Locate every Plasmodium falciparum-infected red blood cell.
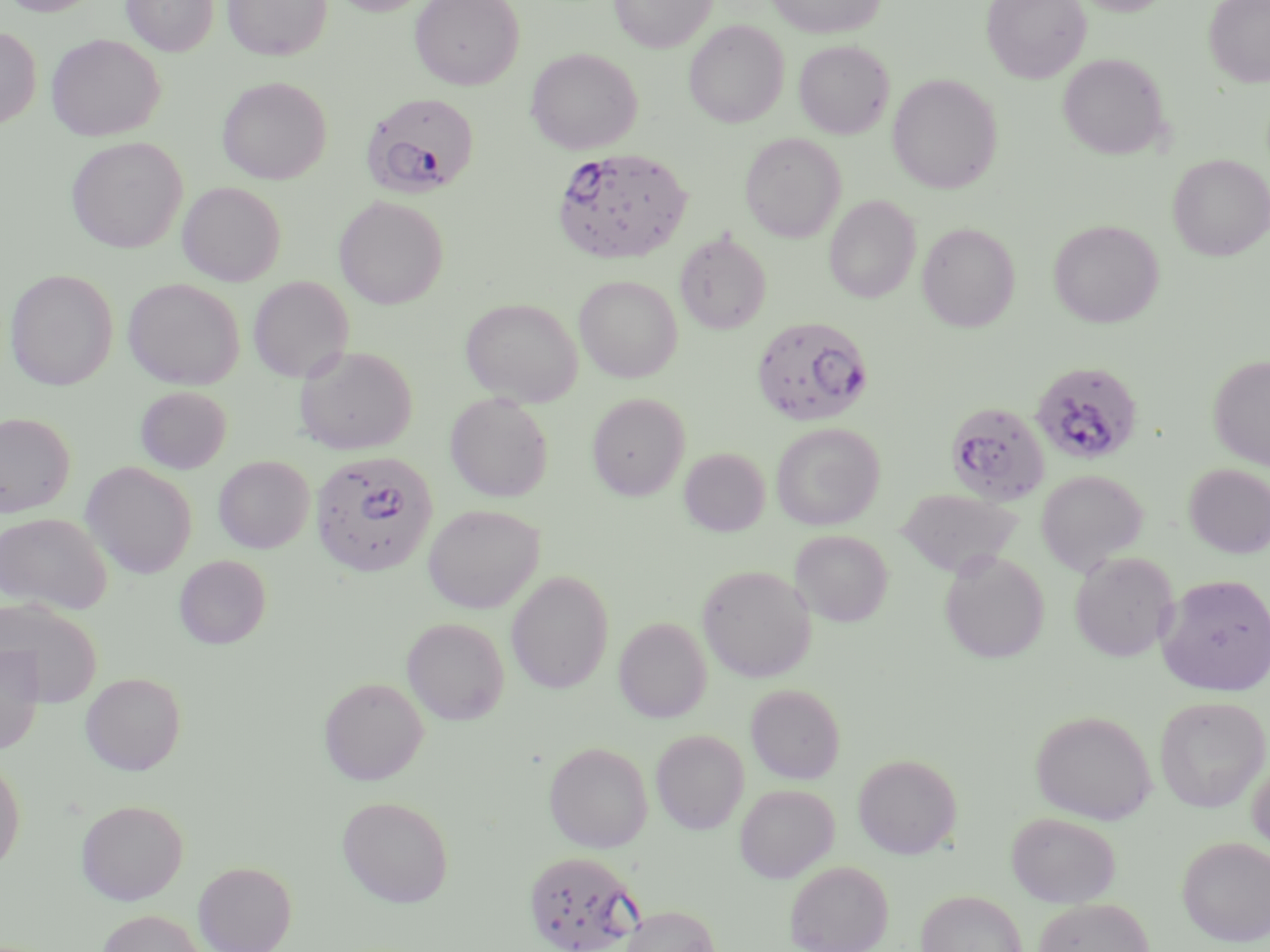

Approximate bounding boxes as (x1, y1, x2, y2) in pixels.
Plasmodium falciparum-infected red blood cells: (361, 92, 478, 198), (550, 147, 693, 264), (751, 315, 873, 427), (1029, 360, 1144, 467), (944, 400, 1052, 503), (310, 450, 438, 578), (523, 849, 642, 952).

Uninfected red blood cell locations: (3, 0, 101, 16), (122, 0, 219, 56), (223, 0, 331, 61), (329, 0, 435, 15), (410, 0, 524, 89), (610, 0, 715, 53), (767, 0, 885, 38), (982, 0, 1091, 83), (1071, 0, 1176, 15), (1204, 0, 1270, 87), (684, 20, 789, 128), (0, 27, 42, 129), (46, 34, 164, 141), (794, 40, 893, 138), (526, 47, 643, 154), (1057, 53, 1170, 159), (887, 73, 1003, 194), (217, 77, 331, 184), (739, 132, 846, 242), (66, 137, 187, 254), (1168, 154, 1270, 260), (177, 181, 286, 286), (824, 195, 920, 303), (334, 196, 449, 309), (1048, 219, 1164, 328), (917, 222, 1020, 332), (675, 231, 771, 334), (4, 269, 118, 390), (574, 275, 683, 383), (247, 276, 354, 383), (124, 278, 244, 389), (460, 298, 582, 406), (294, 345, 418, 454), (1207, 354, 1270, 470), (135, 386, 232, 474), (445, 392, 554, 502), (587, 392, 690, 500), (0, 412, 76, 518), (771, 422, 885, 530), (679, 448, 770, 536), (213, 456, 315, 553), (81, 461, 197, 579), (1183, 463, 1270, 558), (1036, 470, 1147, 574), (896, 488, 1023, 577), (423, 504, 544, 613), (0, 513, 112, 614), (790, 529, 893, 627), (939, 549, 1050, 663), (1070, 551, 1178, 661), (174, 555, 271, 649), (698, 565, 815, 682), (506, 570, 614, 694), (1157, 573, 1270, 696), (0, 601, 102, 706), (402, 617, 510, 725), (614, 617, 712, 722), (0, 645, 44, 753), (81, 672, 186, 775), (319, 677, 429, 785), (746, 683, 846, 783), (1155, 696, 1270, 812), (1030, 710, 1156, 824), (651, 728, 750, 834), (544, 741, 653, 853), (853, 753, 962, 859), (0, 756, 25, 873), (1247, 758, 1270, 861), (734, 784, 838, 883), (337, 795, 454, 908), (76, 799, 189, 905), (1006, 812, 1121, 908), (1178, 836, 1270, 947), (785, 860, 893, 952), (193, 861, 297, 952), (916, 890, 1027, 952), (1032, 898, 1155, 952), (620, 905, 721, 952), (98, 909, 206, 951). Slide-level diagnosis: Plasmodium falciparum. Thin blood film. One field of a larger specimen. Captured at 1000x magnification. Optical microscopy. Image is 1270×952 pixels. May-Grünwald-Giemsa stain.